Name the parasite shown.
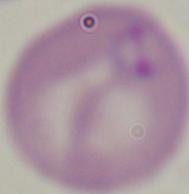

Babesia.

Captured at 1000x magnification. Photomicrograph.